Identify the cell.
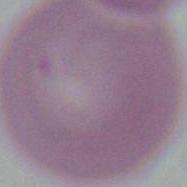
An erythrocyte.

Summary:
  - Modality: photomicrograph
  - Magnification: 1000x